Assess the morphology of the red blood cells.
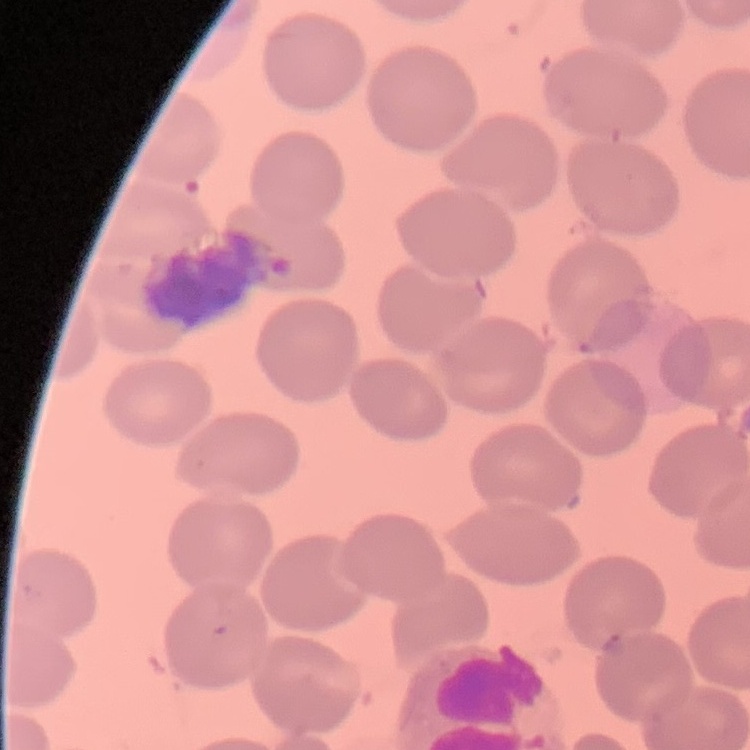

No rouleaux formation.

One tile cut from a larger photomicrograph. Stained with either Field's or Giemsa. Thin blood film.